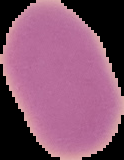

image_type: cell region segmented out of the field of view; surrounding area masked to black
image_size: 124×160 pixels
preparation: thin blood smear
result: no Plasmodium parasites detected